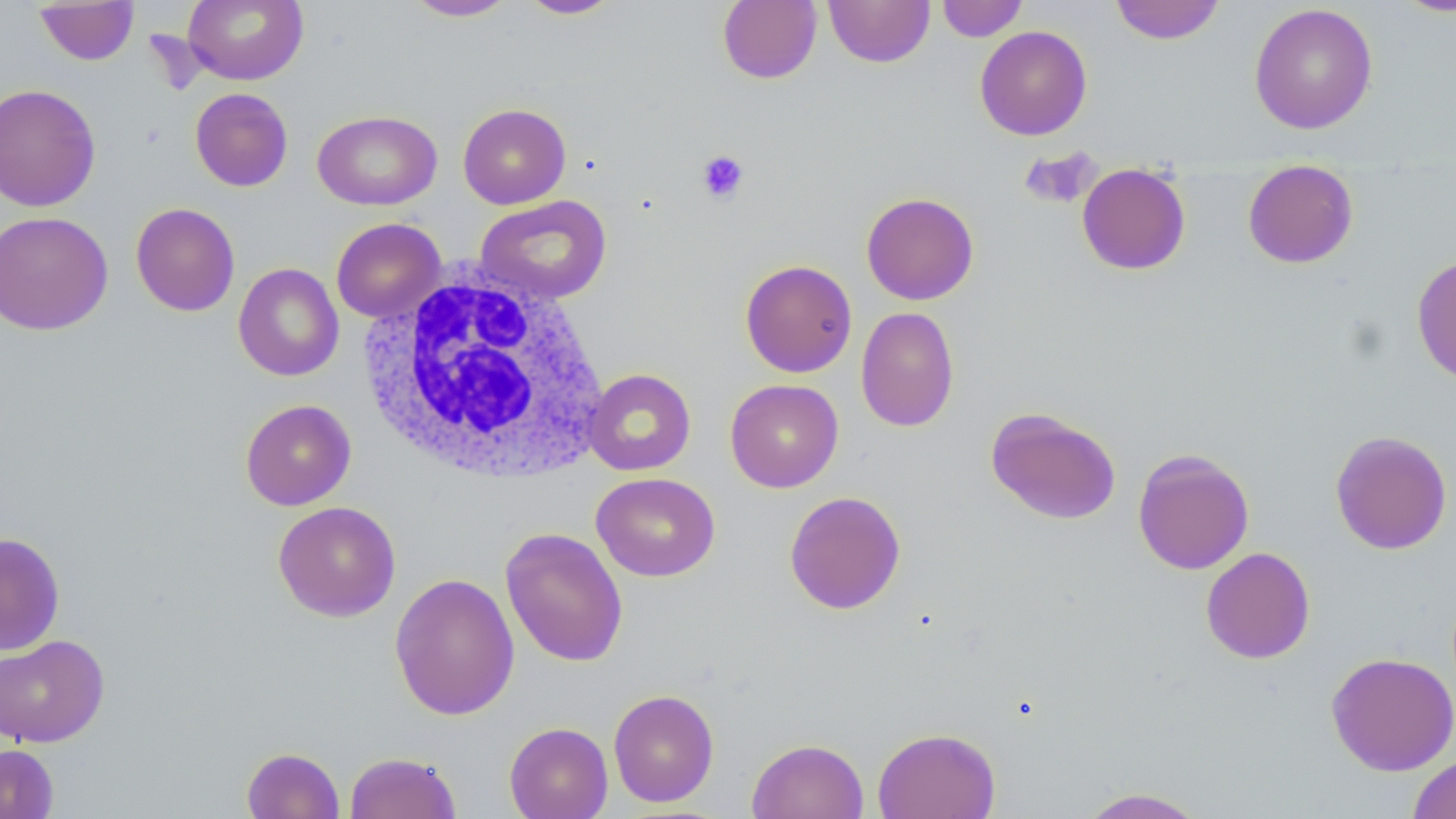

Summary:
  - Coordinate format: approximate bounding boxes as [x1, y1, x2, y2] in pixels
  - Uninfected red blood cell locations: [183, 0, 308, 85], [403, 0, 518, 21], [517, 0, 624, 19], [717, 0, 822, 84], [824, 0, 935, 67], [936, 0, 1028, 41], [1110, 0, 1225, 44], [1393, 0, 1456, 18], [33, 1, 140, 65], [1249, 3, 1378, 135], [975, 25, 1092, 141], [0, 83, 101, 212], [190, 88, 293, 192], [457, 103, 571, 209], [313, 110, 442, 210], [1018, 147, 1102, 210], [1242, 160, 1359, 269], [1077, 164, 1191, 275], [861, 192, 979, 305], [475, 195, 612, 305], [130, 203, 240, 317], [0, 210, 113, 336], [331, 217, 445, 323], [1411, 255, 1456, 386], [739, 259, 857, 378], [233, 262, 344, 382], [856, 306, 959, 432], [583, 368, 696, 476], [725, 378, 844, 492], [240, 399, 356, 510], [985, 406, 1122, 525], [1330, 430, 1453, 555], [1132, 448, 1255, 575], [592, 472, 720, 581], [784, 491, 906, 614], [273, 501, 401, 622], [500, 527, 628, 667], [0, 532, 65, 655], [1200, 547, 1315, 664], [389, 572, 520, 721], [0, 634, 110, 747], [1326, 651, 1456, 776], [608, 689, 720, 807], [505, 714, 721, 814], [504, 722, 613, 819], [873, 727, 1000, 819], [747, 738, 868, 819], [0, 743, 58, 818], [241, 747, 344, 819], [344, 751, 461, 819], [1407, 755, 1456, 819], [1075, 787, 1210, 818]
  - Platelet locations: [697, 149, 749, 204]
  - White blood cell locations: [359, 269, 609, 486]
  - Slide-level diagnosis: no evidence of blood parasites
  - Stain: May-Grünwald-Giemsa
  - Modality: optical microscopy
  - Field of view: one of a larger specimen
  - Preparation: thin blood film
  - Image size: 1456×819 pixels
  - Magnification: 1000x